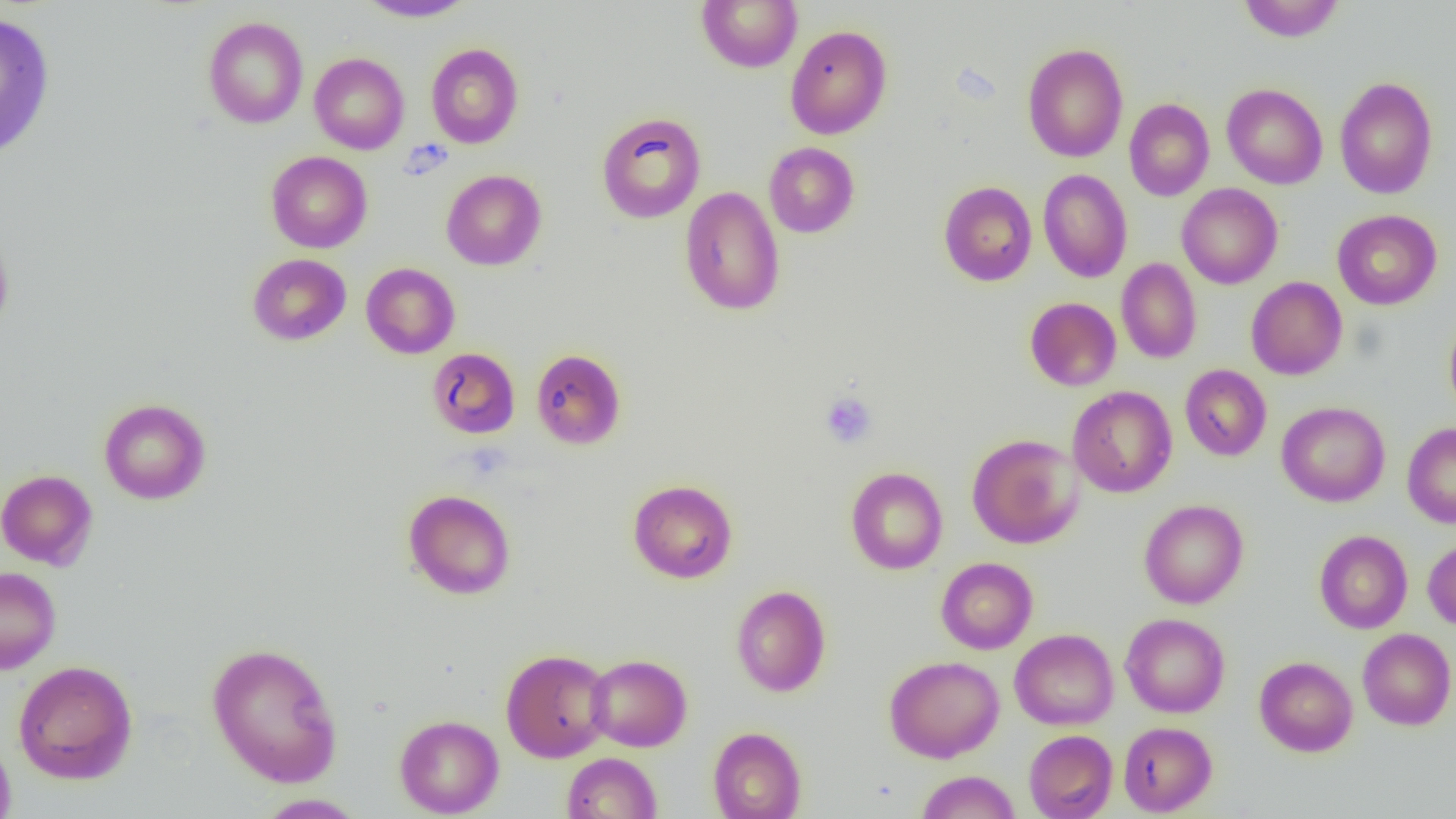
{
  "slide_level_diagnosis": "no evidence of blood parasites",
  "uninfected_red_blood_cell_locations": "approximate bounding boxes as (x1,y1)-(x2,y2) corner pairs in pixels: (358,0)-(475,22), (697,0)-(802,73), (1237,1)-(1345,42), (0,13)-(56,159), (203,16)-(308,128), (785,24)-(892,139), (426,43)-(524,148), (1022,43)-(1128,162), (309,52)-(409,154), (1334,76)-(1438,199), (1221,83)-(1328,189), (1124,98)-(1214,201), (596,112)-(706,224), (764,142)-(860,238), (266,151)-(372,253), (1037,169)-(1133,283), (441,170)-(546,270), (938,181)-(1037,287), (1177,183)-(1283,289), (679,186)-(785,316), (1332,209)-(1442,310), (0,222)-(14,335), (248,253)-(351,345), (1116,259)-(1202,364), (361,263)-(460,358), (1246,276)-(1347,380), (1025,297)-(1121,391), (1444,312)-(1456,420), (426,347)-(520,438), (531,348)-(626,449), (1180,364)-(1271,461), (1068,385)-(1177,498), (98,398)-(211,504), (1277,401)-(1390,506), (1402,422)-(1456,528), (967,433)-(1084,549), (845,467)-(947,574), (0,469)-(98,569), (628,479)-(738,583), (403,489)-(516,599), (1139,499)-(1249,608), (1314,529)-(1413,634), (1423,536)-(1456,630), (936,557)-(1038,654), (0,566)-(61,674), (731,585)-(831,697), (1120,613)-(1230,718), (1010,628)-(1118,730), (1357,628)-(1456,730), (206,641)-(343,787), (501,648)-(613,762), (585,654)-(692,751), (884,655)-(1004,763), (1254,656)-(1357,756), (13,659)-(138,784), (394,715)-(504,817), (1118,721)-(1217,816), (708,726)-(806,819), (1024,729)-(1117,819), (0,732)-(16,819), (562,752)-(662,818), (916,770)-(1020,818), (254,794)-(367,818)",
  "preparation": "thin blood film",
  "modality": "light microscopy",
  "platelet_locations": "approximate bounding boxes as (x1,y1)-(x2,y2) corner pairs in pixels: (819,391)-(878,449)",
  "image_size": "1456×819 pixels",
  "magnification": "1000x",
  "field_of_view": "one of a larger specimen"
}